Outline each Trypanosoma brucei.
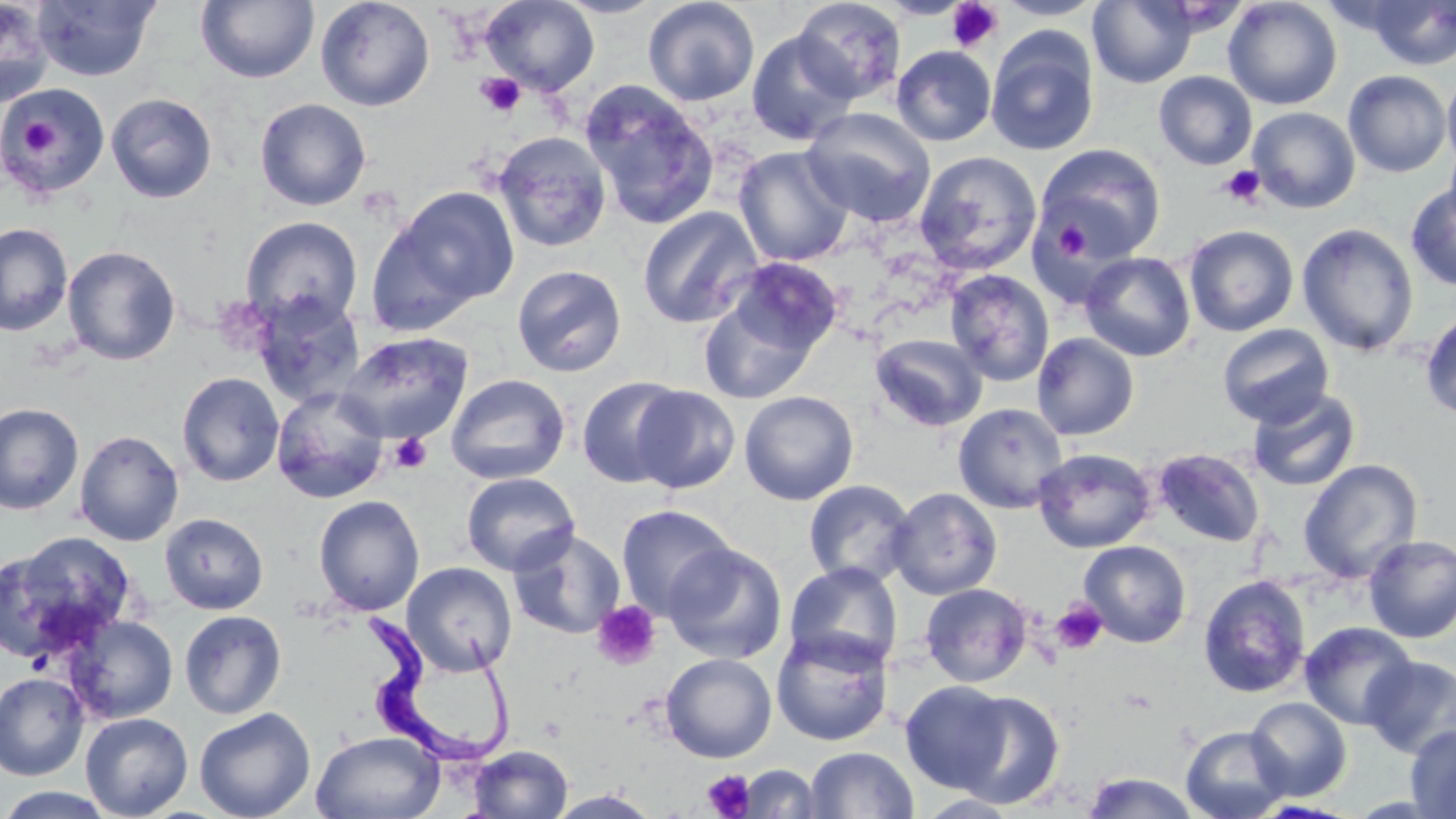

Approximate bounding boxes as (x1,y1)-(x2,y2) corner pairs in pixels.
Trypanosoma brucei: (358,605)-(528,774).

Uninfected red blood cell locations: (195,0)-(319,84), (315,0)-(436,111), (481,0)-(600,95), (552,0)-(668,19), (643,0)-(760,107), (791,0)-(906,103), (993,0)-(1106,20), (1087,0)-(1197,88), (1222,0)-(1343,110), (0,1)-(55,106), (32,1)-(161,82), (1363,1)-(1456,70), (746,30)-(860,145), (985,30)-(1100,156), (891,45)-(997,146), (1343,70)-(1452,178), (1442,70)-(1456,173), (1154,71)-(1257,170), (580,82)-(720,230), (1,83)-(109,198), (106,93)-(218,203), (255,98)-(372,211), (1247,106)-(1360,213), (802,107)-(936,227), (492,131)-(613,253), (1035,143)-(1165,262), (734,146)-(855,267), (914,150)-(1043,276), (1405,182)-(1456,291), (390,186)-(519,309), (637,206)-(763,328), (363,212)-(483,338), (240,216)-(364,328), (0,223)-(73,336), (1296,223)-(1419,356), (1184,225)-(1299,336), (62,245)-(181,365), (1080,252)-(1196,362), (726,257)-(845,359), (512,264)-(627,377), (945,269)-(1055,387), (251,292)-(366,407), (697,293)-(821,404), (1420,308)-(1456,420), (1217,323)-(1335,428), (337,331)-(473,444), (870,333)-(987,432), (1032,333)-(1140,440), (176,372)-(285,487), (445,373)-(570,485), (577,376)-(687,488), (630,386)-(741,493), (271,387)-(390,503), (1248,388)-(1362,492), (739,390)-(859,505), (953,402)-(1068,513), (0,403)-(84,515), (74,429)-(184,546), (1032,447)-(1156,553), (1152,448)-(1266,548), (1298,459)-(1423,584), (461,472)-(581,576), (803,480)-(918,587), (887,487)-(1002,600), (313,495)-(425,616), (616,504)-(738,621), (159,512)-(269,615), (508,527)-(626,640), (1,532)-(137,659), (1362,535)-(1456,643), (1078,540)-(1192,648), (662,542)-(788,665), (402,562)-(517,676), (783,563)-(904,674), (1198,574)-(1311,699), (920,583)-(1033,687), (179,610)-(287,719), (62,614)-(178,724), (1300,621)-(1417,730), (771,628)-(893,746), (660,653)-(777,763), (1361,655)-(1456,758), (0,672)-(89,781), (899,680)-(1015,794), (951,691)-(1066,808), (1245,696)-(1352,801), (194,707)-(315,819), (80,712)-(193,818), (1181,724)-(1291,819), (1405,724)-(1456,819), (310,730)-(446,819), (467,744)-(574,819), (804,746)-(919,819), (737,764)-(824,818), (1080,771)-(1202,818), (0,786)-(117,818), (545,790)-(663,818). Platelet locations: (946,1)-(1003,53), (475,72)-(525,117), (16,115)-(63,163), (1220,165)-(1265,207), (1053,218)-(1089,263), (389,433)-(433,474), (1050,599)-(1108,655), (592,601)-(662,671), (702,769)-(755,818). Slide-level diagnosis: Trypanosoma brucei. Thin blood smear. May-Grünwald-Giemsa-stained preparation. 1000x magnification. Image is 1456×819 pixels. Optical microscopy. Single field of view.